Classify this cell by malaria status.
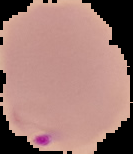
It is parasitized.

{
  "image_size": "133×154 pixels",
  "image_type": "cell region segmented out of the field of view; surrounding area masked to black",
  "preparation": "thin blood smear"
}